Locate every Plasmodium parasite.
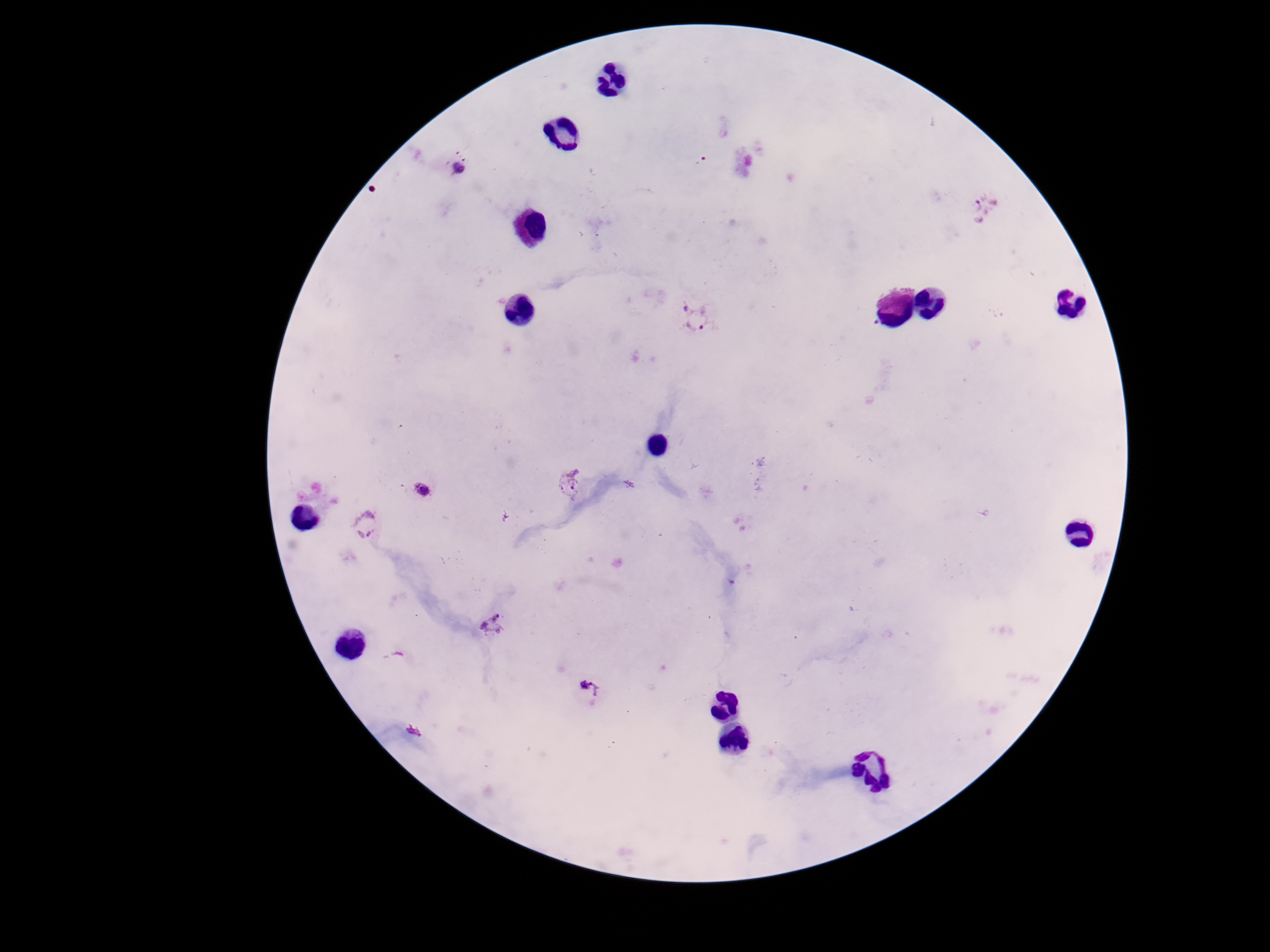

Approximate object centers, in pixels from the top-left corner.
Plasmodium parasites: (x=460, y=167), (x=981, y=208), (x=698, y=319), (x=569, y=482), (x=422, y=490), (x=364, y=524), (x=492, y=625), (x=591, y=692).

patient_malaria_status: infected
stain: Giemsa
capture: smartphone camera through the microscope eyepiece
preparation: thick blood smear
field_of_view: one from this slide
magnification: 100x
image_size: 1270×952 pixels